Classify this cell by malaria status.
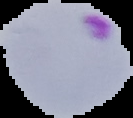
It is parasitized.

Summary:
  - Preparation: thin blood smear
  - Image size: 133×118 pixels
  - Image type: cell region segmented out of the field of view; surrounding area masked to black